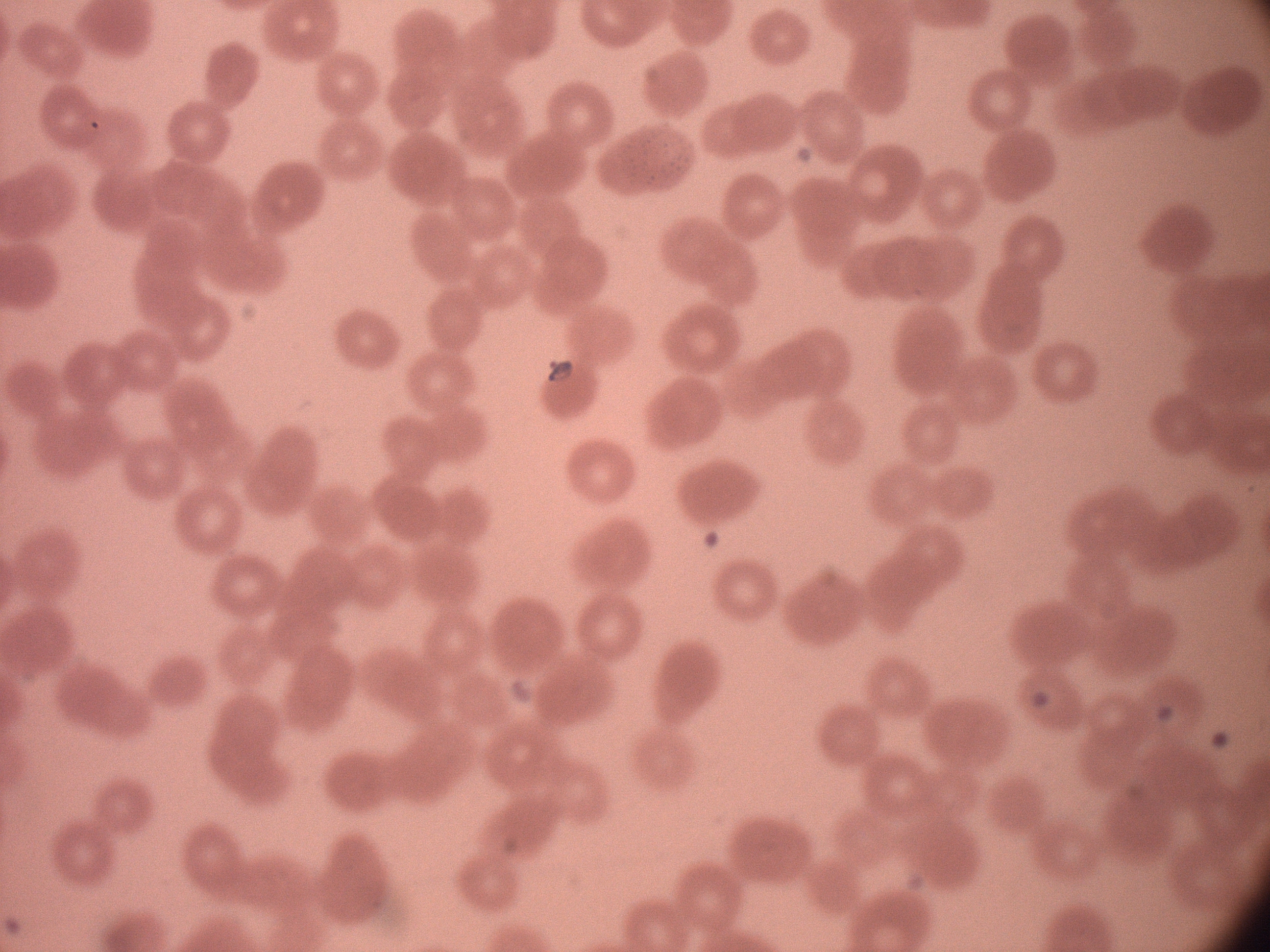

Approximate bounding boxes as (x1, y1, x2, y2) in pixels, from the source annotation, which is not necessarily exhaustive.
Summary:
  - Ring form locations: (531, 350, 582, 392)
  - Field of view: single
  - Stain: Giemsa
  - Magnification: 100x
  - Species: Plasmodium falciparum
  - Microscope: Leica DM2000 with built-in camera
  - Preparation: thin blood film
  - Image size: 1270×952 pixels